Locate every uninfected red blood cell.
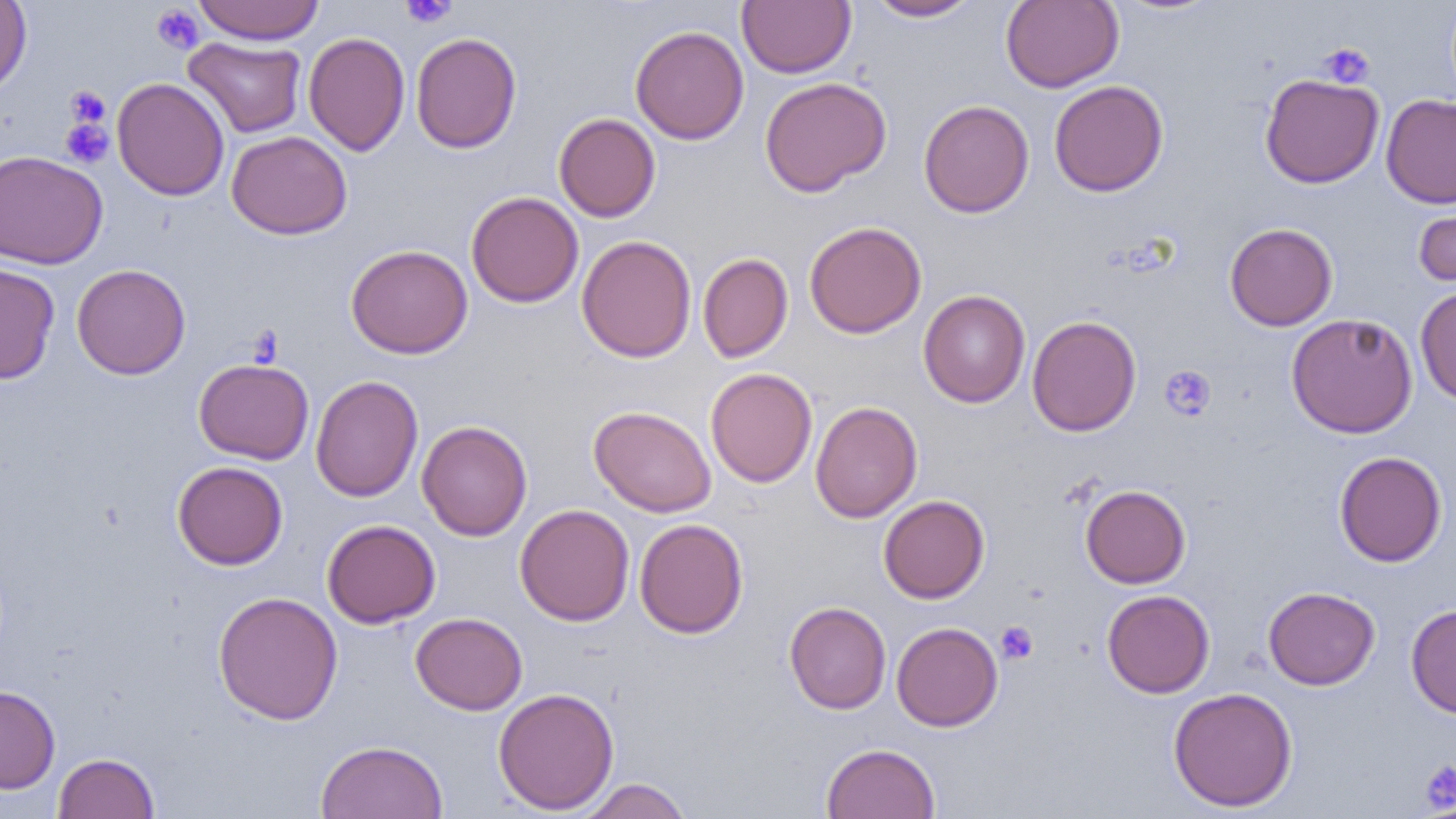
Approximate bounding boxes as named x1/y1/x2/y2 corners in pixels.
Uninfected red blood cells: (x1=0, y1=0, x2=32, y2=97), (x1=191, y1=0, x2=325, y2=45), (x1=737, y1=0, x2=855, y2=78), (x1=865, y1=0, x2=981, y2=22), (x1=1000, y1=0, x2=1123, y2=92), (x1=630, y1=25, x2=749, y2=144), (x1=303, y1=31, x2=410, y2=156), (x1=411, y1=31, x2=522, y2=153), (x1=183, y1=36, x2=307, y2=138), (x1=1259, y1=72, x2=1385, y2=189), (x1=759, y1=76, x2=891, y2=197), (x1=112, y1=77, x2=229, y2=201), (x1=1049, y1=80, x2=1168, y2=197), (x1=1381, y1=94, x2=1456, y2=209), (x1=918, y1=99, x2=1034, y2=218), (x1=554, y1=113, x2=661, y2=222), (x1=226, y1=131, x2=352, y2=240), (x1=0, y1=150, x2=108, y2=269), (x1=466, y1=191, x2=584, y2=308), (x1=1414, y1=194, x2=1456, y2=290), (x1=804, y1=220, x2=927, y2=338), (x1=1225, y1=222, x2=1338, y2=331), (x1=576, y1=235, x2=697, y2=362), (x1=346, y1=244, x2=473, y2=358), (x1=697, y1=253, x2=793, y2=363), (x1=0, y1=262, x2=60, y2=385), (x1=71, y1=263, x2=190, y2=379), (x1=1415, y1=285, x2=1456, y2=405), (x1=918, y1=289, x2=1031, y2=408), (x1=1285, y1=313, x2=1418, y2=438), (x1=1026, y1=315, x2=1142, y2=436), (x1=193, y1=357, x2=314, y2=464), (x1=705, y1=368, x2=818, y2=487), (x1=310, y1=376, x2=423, y2=501), (x1=810, y1=401, x2=923, y2=523), (x1=588, y1=405, x2=717, y2=517), (x1=417, y1=420, x2=533, y2=541), (x1=1334, y1=451, x2=1447, y2=567), (x1=173, y1=461, x2=288, y2=569), (x1=1080, y1=484, x2=1190, y2=588), (x1=878, y1=495, x2=990, y2=603), (x1=514, y1=504, x2=635, y2=625), (x1=633, y1=518, x2=748, y2=638), (x1=322, y1=519, x2=441, y2=628), (x1=1263, y1=586, x2=1380, y2=690), (x1=1102, y1=589, x2=1215, y2=697), (x1=212, y1=591, x2=343, y2=725), (x1=784, y1=601, x2=891, y2=714), (x1=1406, y1=604, x2=1456, y2=718), (x1=410, y1=612, x2=527, y2=715), (x1=891, y1=621, x2=1003, y2=731), (x1=0, y1=685, x2=60, y2=794), (x1=492, y1=686, x2=620, y2=814), (x1=1167, y1=687, x2=1298, y2=813), (x1=314, y1=739, x2=449, y2=819), (x1=821, y1=742, x2=940, y2=819), (x1=53, y1=752, x2=159, y2=818), (x1=576, y1=778, x2=694, y2=819).

Summary:
  - Platelet locations: (x1=400, y1=0, x2=457, y2=28), (x1=151, y1=5, x2=204, y2=53), (x1=1319, y1=43, x2=1375, y2=88), (x1=65, y1=86, x2=110, y2=129), (x1=60, y1=116, x2=114, y2=169), (x1=1160, y1=364, x2=1216, y2=421), (x1=996, y1=621, x2=1038, y2=664), (x1=1419, y1=760, x2=1456, y2=815)
  - Slide-level diagnosis: no evidence of blood parasites
  - Image size: 1456×819 pixels
  - Magnification: 1000x
  - Preparation: thin blood smear
  - Modality: light microscopy
  - Field of view: one of a larger specimen